Report the malaria status of this cell.
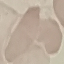
It is uninfected.

Summary:
  - Preparation: thin blood film
  - Stain: Giemsa
  - Capture: smartphone camera at the microscope eyepiece
  - Image type: cell patch, automatically extracted from a larger field of view and resized to 64 × 64 pixels